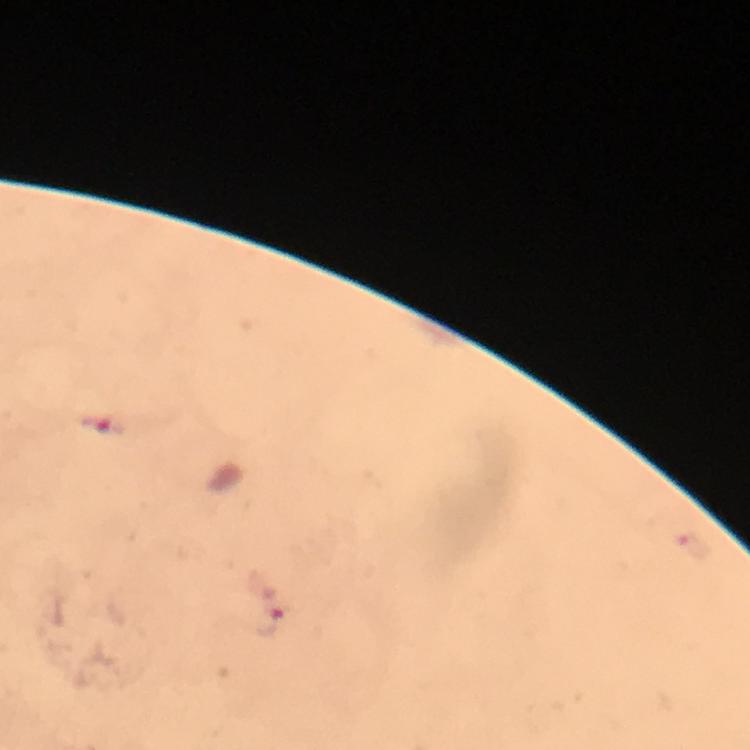 Approximate centers as {x, y} in pixels. Malaria parasite locations: {102, 429}, {271, 624}. Image is 750×750 pixels. Smartphone photograph taken through a microscope. Immersion oil was used. Thick smear. Giemsa stain. A crop from one field of view. 100x magnification. From a malaria diagnostic workup.